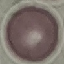
Summary:
  - Result: no malaria parasites seen
  - Stain: Giemsa
  - Capture: smartphone camera at the microscope eyepiece
  - Preparation: thin blood film
  - Image type: automatically extracted cell patch, resized to 64 × 64 pixels